Identify the parasite.
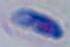
Toxoplasma gondii.

Summary:
  - Modality: photomicrograph
  - Magnification: 1000x